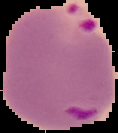
image_size: 118×133 pixels
preparation: thin blood film
image_type: segmented cell region on a black background
result: malaria parasites detected